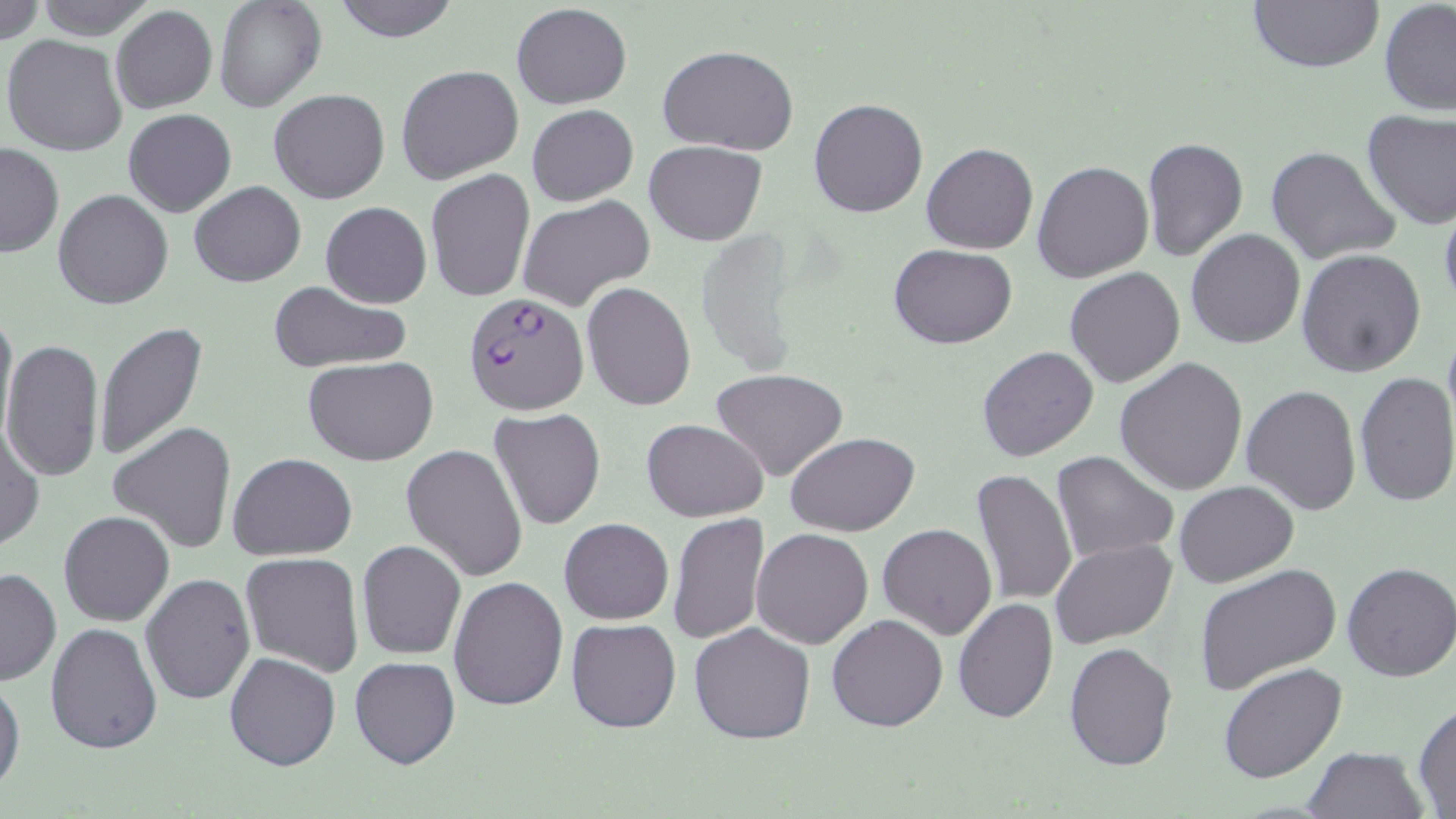
Approximate bounding boxes as (x1,y1)-(x2,y2) corner pairs in pixels. Plasmodium falciparum-infected red blood cell locations: (464,294)-(589,416). Uninfected red blood cell locations: (31,0)-(159,39), (214,0)-(326,112), (331,0)-(460,42), (1247,0)-(1385,74), (0,1)-(46,47), (1379,1)-(1456,116), (511,3)-(631,109), (110,5)-(218,115), (3,34)-(128,155), (658,44)-(799,156), (396,65)-(525,184), (269,90)-(391,205), (809,99)-(928,219), (527,104)-(637,205), (123,108)-(236,217), (1361,109)-(1456,230), (1142,137)-(1248,260), (646,140)-(766,246), (0,142)-(63,258), (921,142)-(1038,254), (1265,145)-(1402,266), (1032,161)-(1154,283), (425,169)-(535,302), (189,180)-(306,287), (54,189)-(174,309), (516,195)-(655,312), (1438,199)-(1456,313), (321,202)-(432,307), (1185,228)-(1305,349), (695,230)-(803,376), (890,244)-(1017,347), (1296,249)-(1425,377), (1064,267)-(1186,388), (267,280)-(411,373), (581,282)-(697,411), (0,302)-(18,445), (93,321)-(208,463), (1442,321)-(1456,441), (2,338)-(104,482), (977,345)-(1100,463), (306,357)-(439,466), (1115,358)-(1248,495), (711,368)-(848,481), (1354,370)-(1456,507), (1242,385)-(1362,516), (488,408)-(605,531), (642,418)-(768,522), (0,419)-(44,553), (108,421)-(238,554), (787,432)-(919,536), (402,444)-(529,582), (1052,451)-(1178,565), (228,453)-(358,560), (971,469)-(1077,611), (1174,480)-(1298,587), (58,511)-(175,626), (668,513)-(770,645), (558,517)-(674,623), (878,523)-(997,640), (750,527)-(874,648), (1050,538)-(1178,647), (357,540)-(466,659), (240,553)-(365,677), (1341,562)-(1456,682), (1193,564)-(1341,696), (0,566)-(60,686), (141,572)-(255,706), (448,576)-(568,710), (953,599)-(1058,723), (827,614)-(947,731), (565,618)-(681,733), (45,622)-(162,755), (689,622)-(816,744), (1064,642)-(1178,770), (225,652)-(341,770), (350,656)-(460,770), (1219,663)-(1348,784), (0,673)-(24,798), (1412,702)-(1456,815), (1303,747)-(1427,818). Slide-level diagnosis: Plasmodium falciparum. Thin blood film. 1000x magnification. May-Grünwald-Giemsa-stained preparation. Single field of view. Light microscopy. Image is 1456×819 pixels.